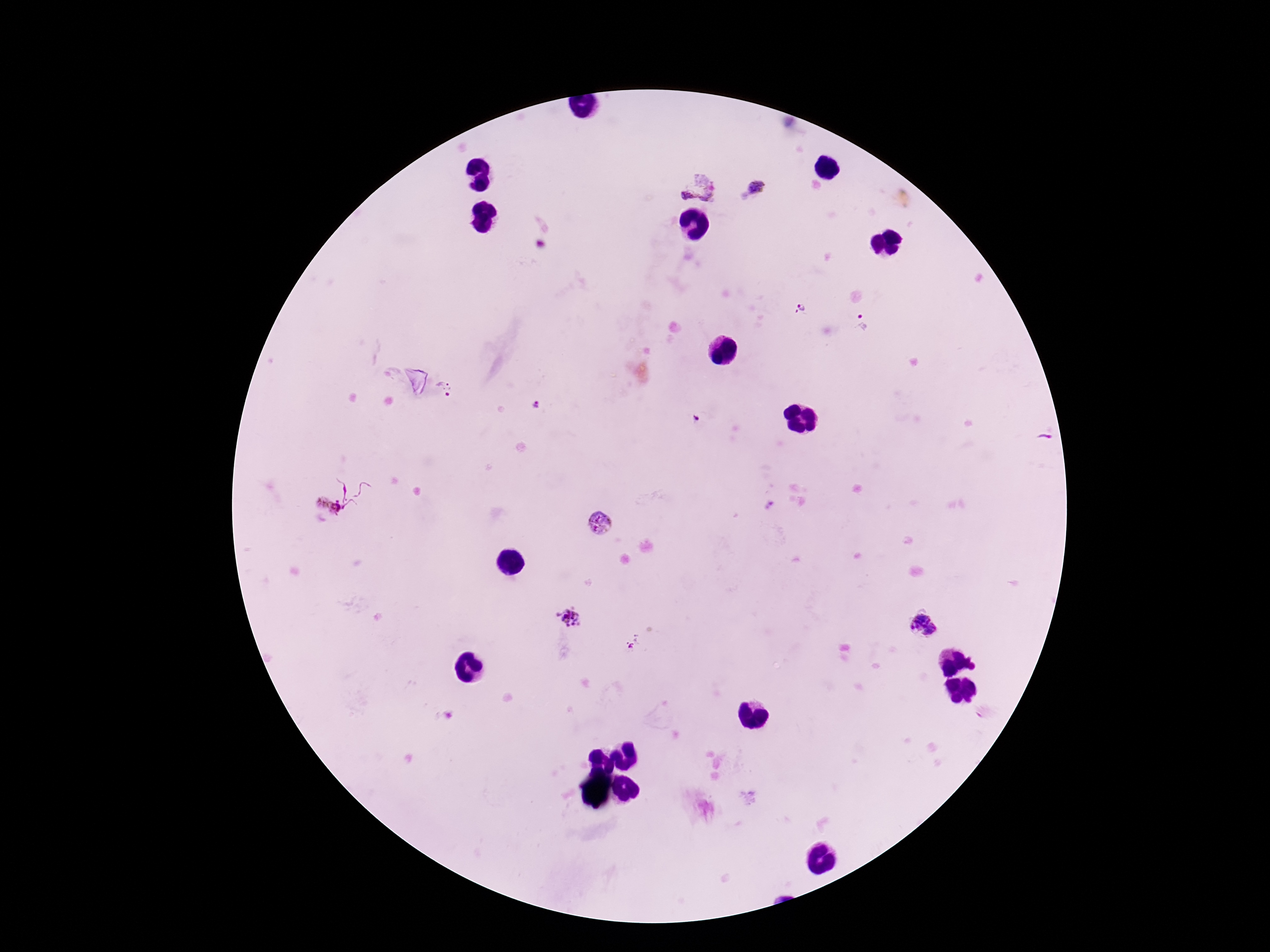

Approximate centers as [x, y] in pixels. Plasmodium parasite locations: [698, 185], [756, 187], [798, 307], [863, 322], [447, 388], [535, 403], [696, 419], [358, 489], [326, 504], [770, 504], [600, 522], [573, 618], [925, 623], [633, 643]. Giemsa-stained preparation. Image is 1270×952 pixels. Single field of view. Patient malaria status: infected. Photographed through the microscope eyepiece with a smartphone camera. Thick blood film. 100x magnification.